Describe the morphology of the red blood cells.
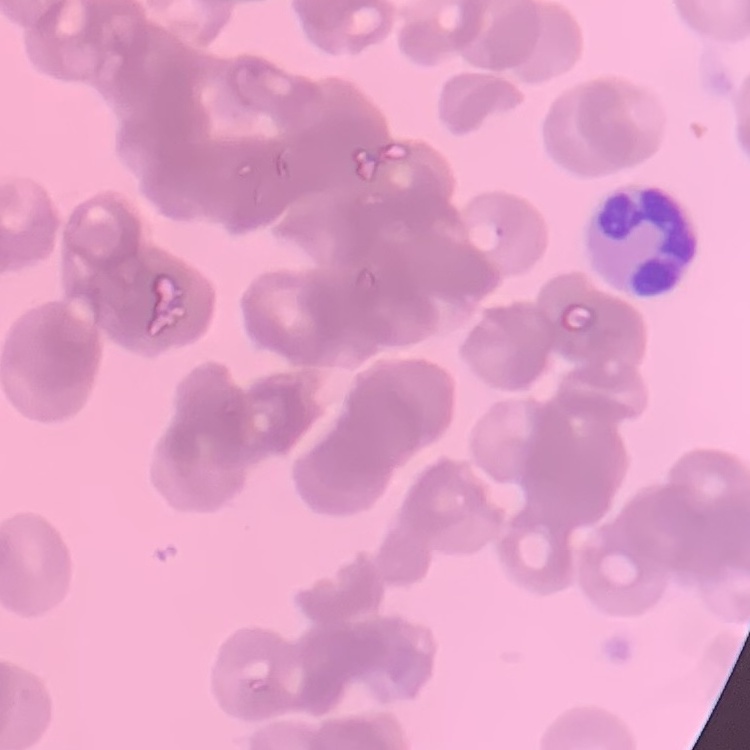
They show rouleaux formation.

Stained with either Field's or Giemsa. Thin blood smear. One tile cut from a larger photomicrograph.